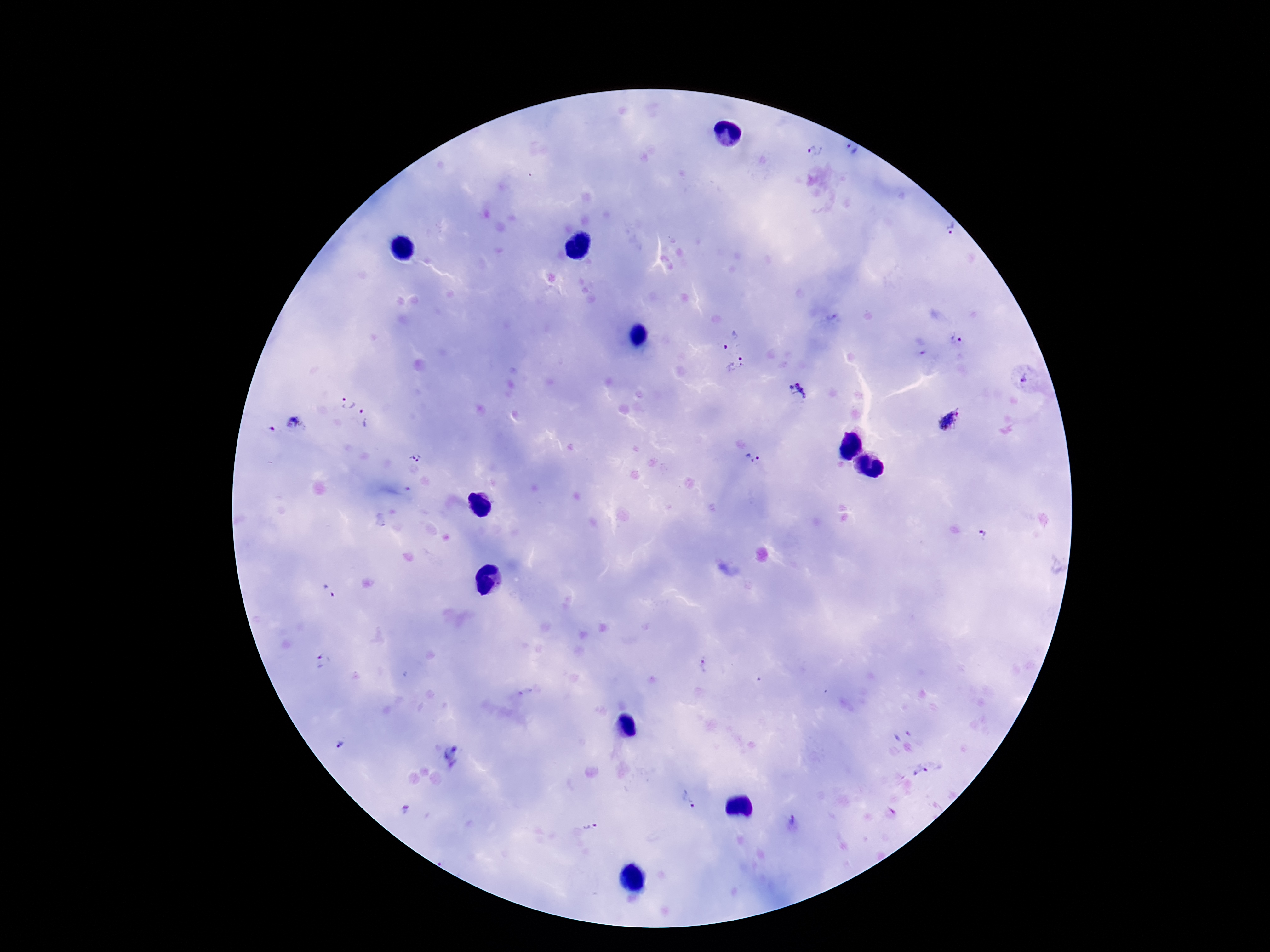

Approximate centers as (x, y) in pixels.
Summary:
  - Plasmodium parasite locations: (851, 151), (815, 152), (949, 229), (729, 337), (956, 341), (919, 347), (737, 365), (1026, 380), (798, 391), (345, 403), (365, 418), (951, 421), (294, 424), (272, 429), (416, 456), (753, 457), (984, 535), (328, 591), (323, 661), (704, 666), (341, 744), (449, 750), (921, 772), (689, 799), (405, 811), (792, 818), (590, 827)
  - Patient malaria status: infected
  - Preparation: thick blood film
  - Magnification: 100x
  - Stain: Giemsa
  - Image size: 1270×952 pixels
  - Capture: smartphone camera through the microscope eyepiece
  - Field of view: single